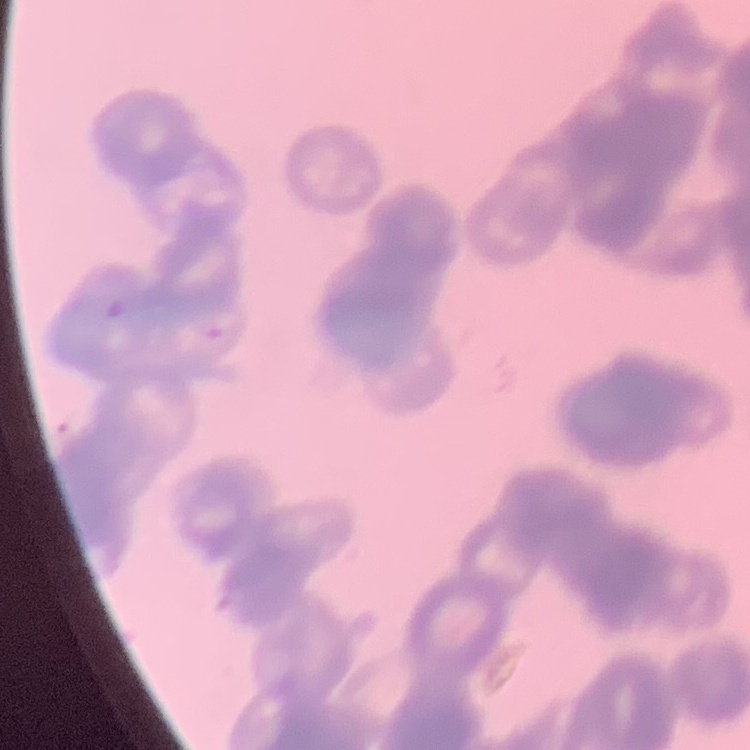
The erythrocytes show rouleaux formation. Thin blood film. One tile cut from a larger photomicrograph. Stained with either Field's or Giemsa.